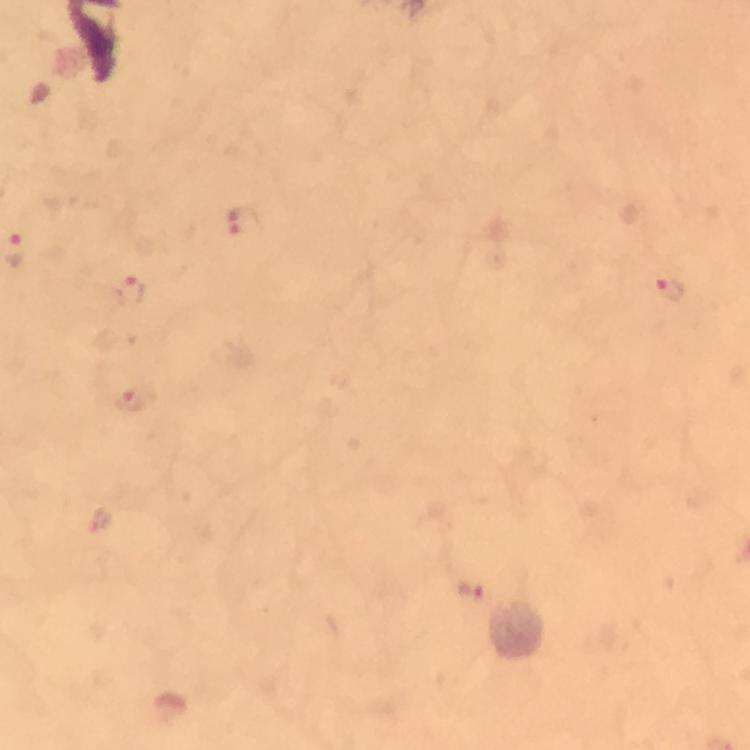

Approximate centers as {x, y} in pixels.
Summary:
  - Plasmodium parasite locations: {243, 222}, {669, 289}, {130, 292}, {127, 400}, {472, 593}
  - Magnification: 100x
  - Cropped from: one field of view
  - Context: from a malaria diagnostic workup
  - Stain: Giemsa
  - Image size: 750×750 pixels
  - Immersion oil: used
  - Capture: smartphone mounted on the microscope
  - Preparation: thick smear